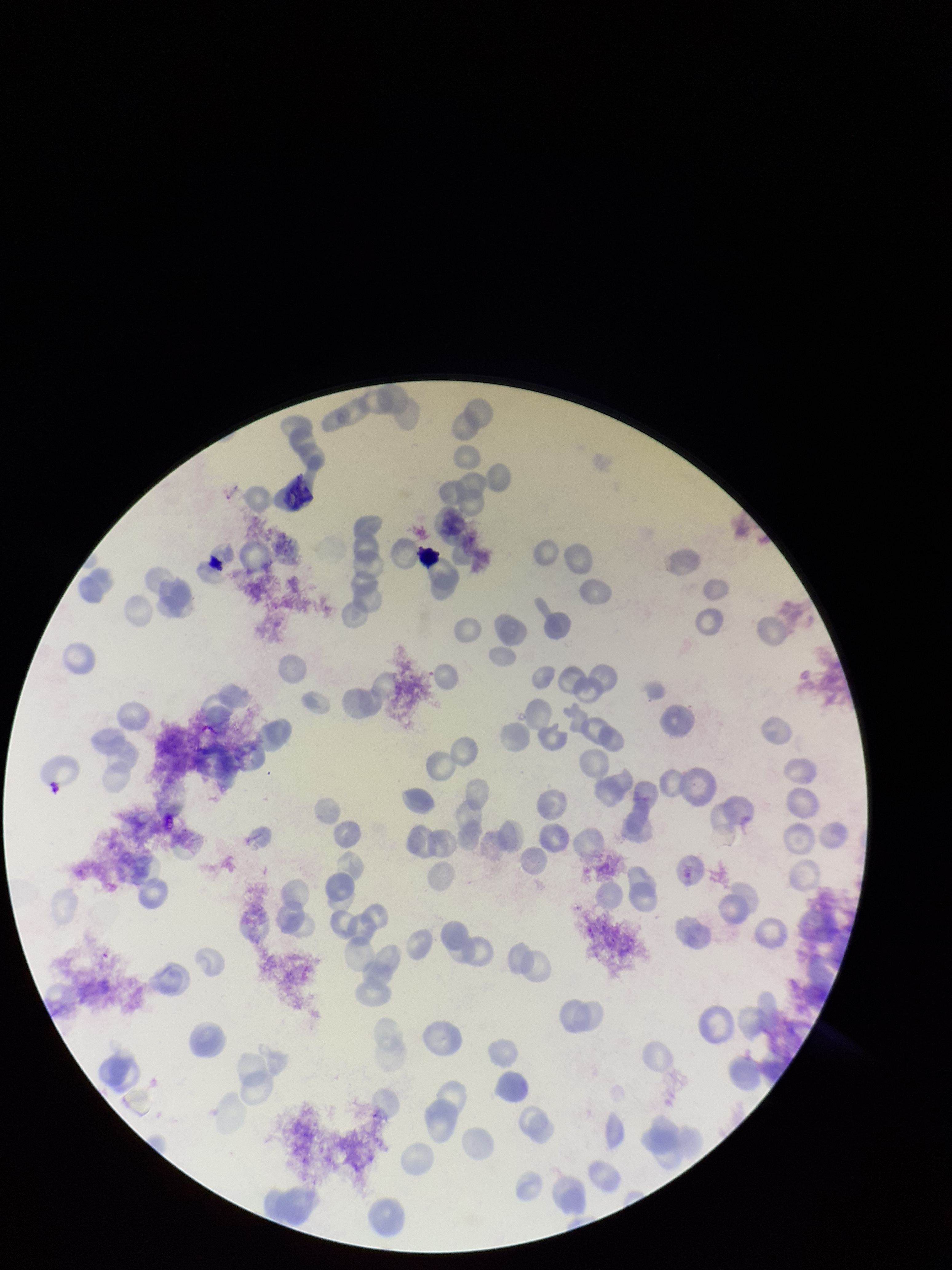

{
  "red_blood_cell_count": 156,
  "species_reported_for_this_patient": "Plasmodium vivax",
  "preparation": "thin smear",
  "capture": "smartphone photograph through the microscope eyepiece",
  "patient_malaria_status": "positive",
  "stain": "Giemsa",
  "parasitized_red_blood_cells": "none detected",
  "image_size": "952×1270 pixels",
  "parasitized_red_blood_cell_count": 0,
  "field_of_view": "single"
}